Report the malaria status of this cell.
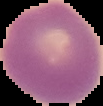

Uninfected.

preparation = thin blood film
image type = segmented cell region on a black background
image size = 103×106 pixels